Locate and identify every blood parasite.
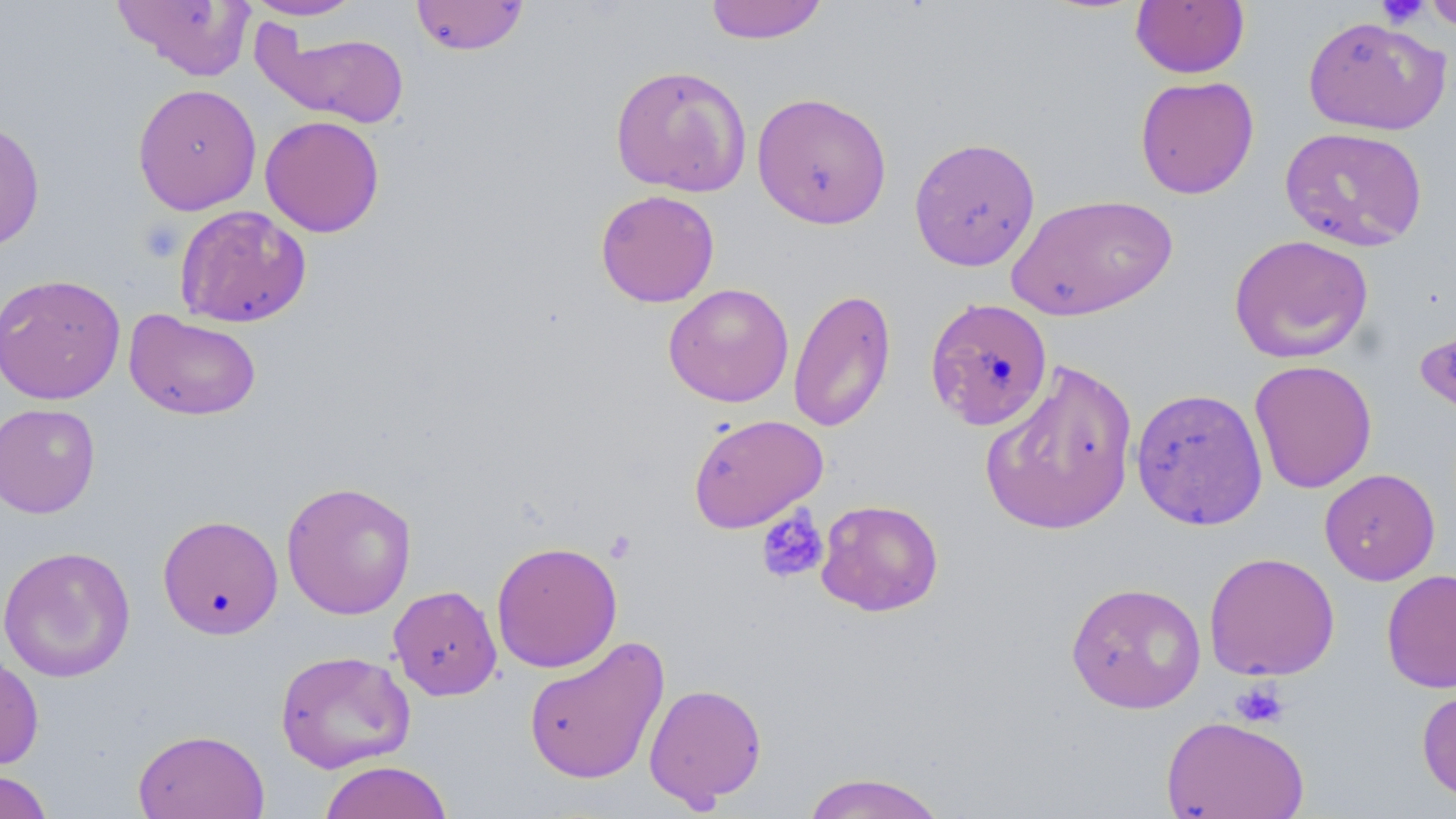

No blood parasites seen.

Summary:
  - Coordinate format: approximate bounding boxes as named x1/y1/x2/y2 corners in pixels
  - Uninfected red blood cell locations: (x1=113, y1=0, x2=256, y2=81), (x1=242, y1=0, x2=366, y2=21), (x1=411, y1=0, x2=529, y2=56), (x1=704, y1=0, x2=828, y2=45), (x1=1422, y1=0, x2=1456, y2=34), (x1=1130, y1=1, x2=1250, y2=78), (x1=1302, y1=15, x2=1451, y2=136), (x1=257, y1=28, x2=410, y2=129), (x1=610, y1=64, x2=752, y2=197), (x1=1134, y1=75, x2=1259, y2=199), (x1=133, y1=83, x2=262, y2=215), (x1=751, y1=91, x2=892, y2=229), (x1=259, y1=115, x2=385, y2=237), (x1=0, y1=118, x2=46, y2=252), (x1=1279, y1=126, x2=1429, y2=251), (x1=908, y1=136, x2=1041, y2=271), (x1=595, y1=189, x2=720, y2=307), (x1=1006, y1=192, x2=1178, y2=322), (x1=174, y1=204, x2=312, y2=328), (x1=1228, y1=234, x2=1374, y2=364), (x1=0, y1=273, x2=125, y2=404), (x1=663, y1=283, x2=795, y2=407), (x1=788, y1=286, x2=896, y2=433), (x1=925, y1=296, x2=1054, y2=432), (x1=124, y1=309, x2=262, y2=420), (x1=980, y1=359, x2=1139, y2=536), (x1=1249, y1=359, x2=1377, y2=494), (x1=1130, y1=386, x2=1268, y2=530), (x1=1, y1=403, x2=101, y2=519), (x1=688, y1=413, x2=828, y2=533), (x1=1319, y1=468, x2=1440, y2=585), (x1=280, y1=480, x2=417, y2=619), (x1=815, y1=499, x2=944, y2=616), (x1=157, y1=514, x2=284, y2=639), (x1=490, y1=540, x2=623, y2=673), (x1=0, y1=545, x2=136, y2=683), (x1=1204, y1=551, x2=1340, y2=681), (x1=1381, y1=569, x2=1456, y2=693), (x1=1066, y1=581, x2=1206, y2=714), (x1=388, y1=585, x2=502, y2=701), (x1=523, y1=636, x2=669, y2=784), (x1=274, y1=649, x2=416, y2=773), (x1=0, y1=651, x2=44, y2=771), (x1=644, y1=682, x2=767, y2=808), (x1=1417, y1=682, x2=1456, y2=806), (x1=1160, y1=715, x2=1309, y2=818), (x1=132, y1=728, x2=269, y2=818), (x1=318, y1=760, x2=453, y2=819), (x1=0, y1=769, x2=53, y2=819), (x1=800, y1=772, x2=949, y2=818)
  - Platelet locations: (x1=1375, y1=0, x2=1430, y2=28), (x1=138, y1=219, x2=185, y2=262), (x1=755, y1=505, x2=830, y2=585), (x1=604, y1=530, x2=637, y2=564), (x1=1230, y1=680, x2=1290, y2=728)
  - Slide-level diagnosis: no evidence of blood parasites
  - Preparation: thin blood smear
  - Modality: optical microscopy
  - Image size: 1456×819 pixels
  - Stain: May-Grünwald-Giemsa
  - Magnification: 1000x
  - Field of view: single